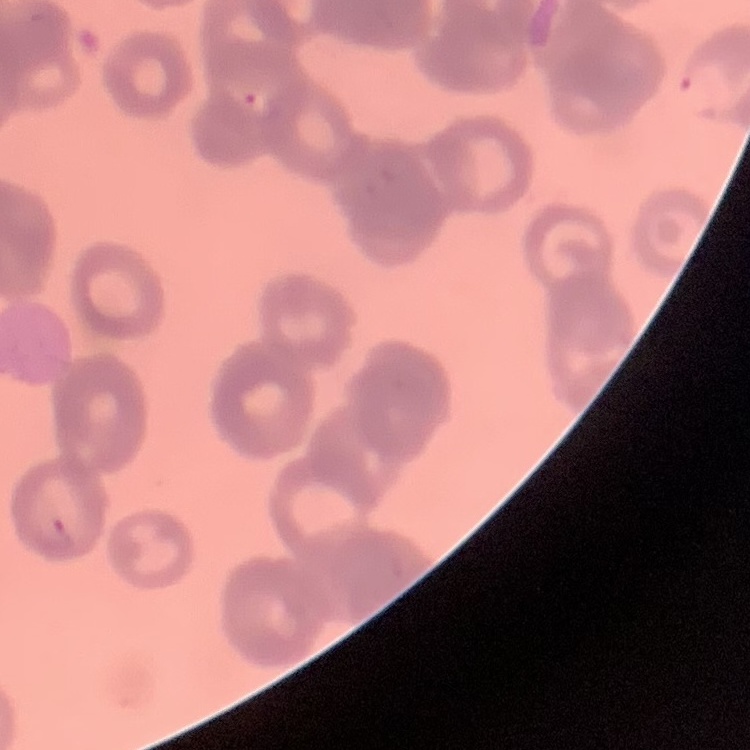
Summary:
  - Erythrocyte morphology: rouleaux formation
  - Stain: Field's or Giemsa
  - Image type: one tile cut from a larger photomicrograph
  - Preparation: thin blood film